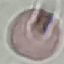
Summary:
  - Malaria status: uninfected
  - Capture: smartphone through the microscope eyepiece
  - Preparation: thin blood smear
  - Stain: Giemsa
  - Image type: automatically extracted cell patch, resized to 64 × 64 pixels